Name the blood parasite species.
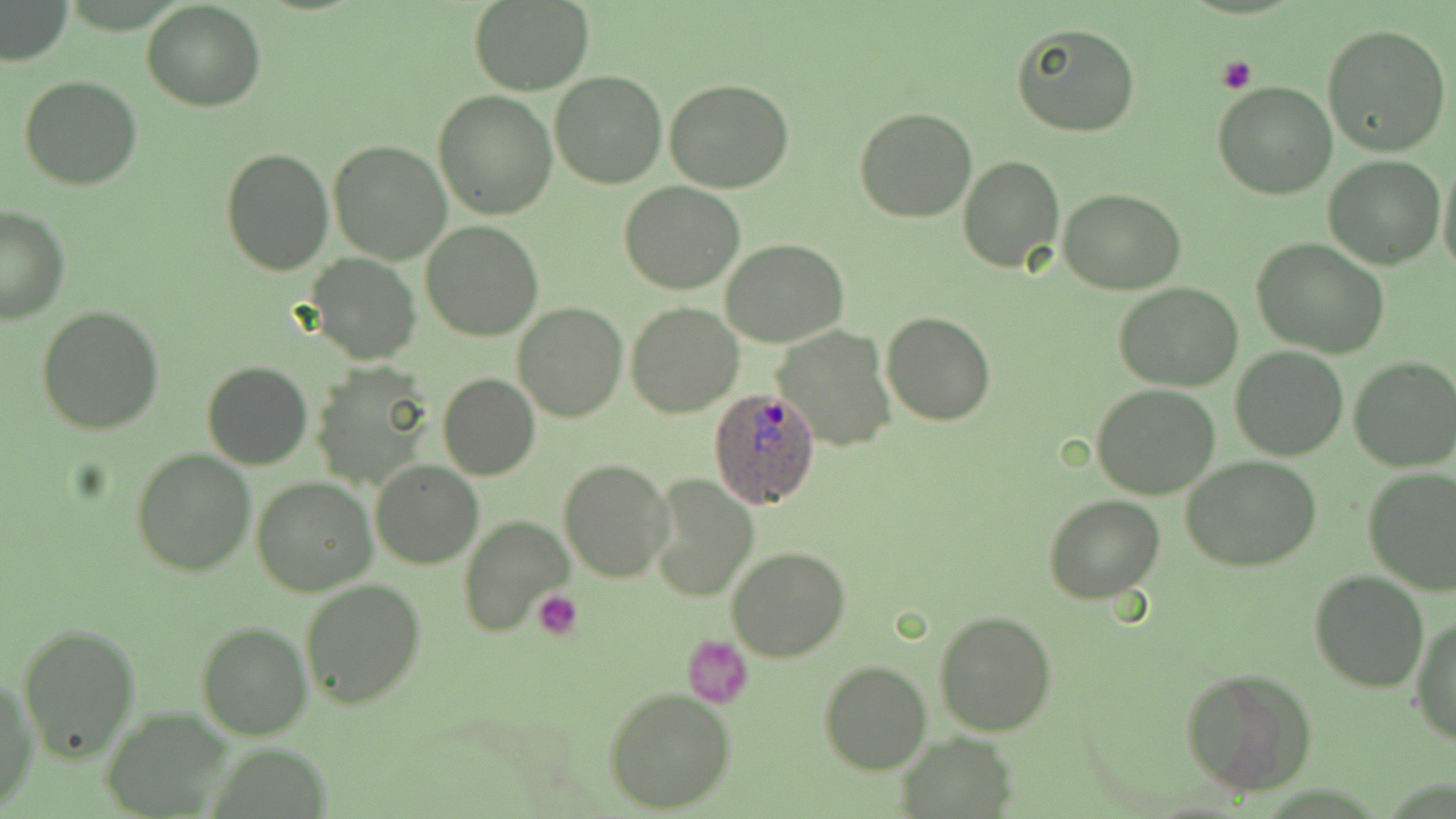

Plasmodium ovale.

Approximate bounding boxes as (x1,y1)-(x2,y2) corner pairs in pixels. Uninfected red blood cell locations: (1,1)-(73,65), (142,1)-(267,112), (467,1)-(594,94), (1322,23)-(1453,158), (1012,24)-(1140,138), (550,71)-(666,187), (18,74)-(143,190), (664,78)-(795,194), (1213,82)-(1338,200), (433,91)-(557,220), (854,106)-(978,223), (329,139)-(450,263), (220,148)-(334,276), (1323,155)-(1446,270), (1437,156)-(1456,279), (958,157)-(1064,274), (620,181)-(745,295), (1059,188)-(1186,293), (0,205)-(69,326), (421,219)-(543,339), (1252,236)-(1389,358), (722,239)-(848,348), (307,254)-(420,365), (1115,282)-(1244,392), (513,301)-(628,423), (627,302)-(744,418), (37,305)-(165,435), (881,311)-(996,426), (772,327)-(895,452), (1231,346)-(1348,461), (1350,357)-(1456,473), (203,360)-(312,470), (311,365)-(434,488), (438,373)-(540,480), (1091,383)-(1220,499), (131,448)-(254,576), (1181,455)-(1323,572), (370,459)-(484,570), (557,459)-(673,584), (1363,467)-(1456,594), (650,475)-(758,600), (251,476)-(376,596), (1044,494)-(1164,603), (461,516)-(573,640), (726,546)-(851,662), (1308,570)-(1429,692), (298,578)-(427,709), (934,609)-(1056,737), (1412,613)-(1456,744), (195,620)-(313,740), (18,622)-(141,761), (683,634)-(752,706), (817,660)-(933,775), (1179,667)-(1315,797), (0,679)-(37,811), (604,688)-(735,812), (100,707)-(236,815), (897,732)-(1020,816). Platelet locations: (1215,56)-(1256,93), (533,589)-(583,641). Plasmodium ovale-infected red blood cell locations: (707,388)-(823,510). Thin blood smear. Optical microscopy. One field of a larger specimen. Image is 1456×819 pixels. 1000x magnification. May-Grünwald-Giemsa stain.